Give the position of every Plasmodium parasite and every leukocyte.
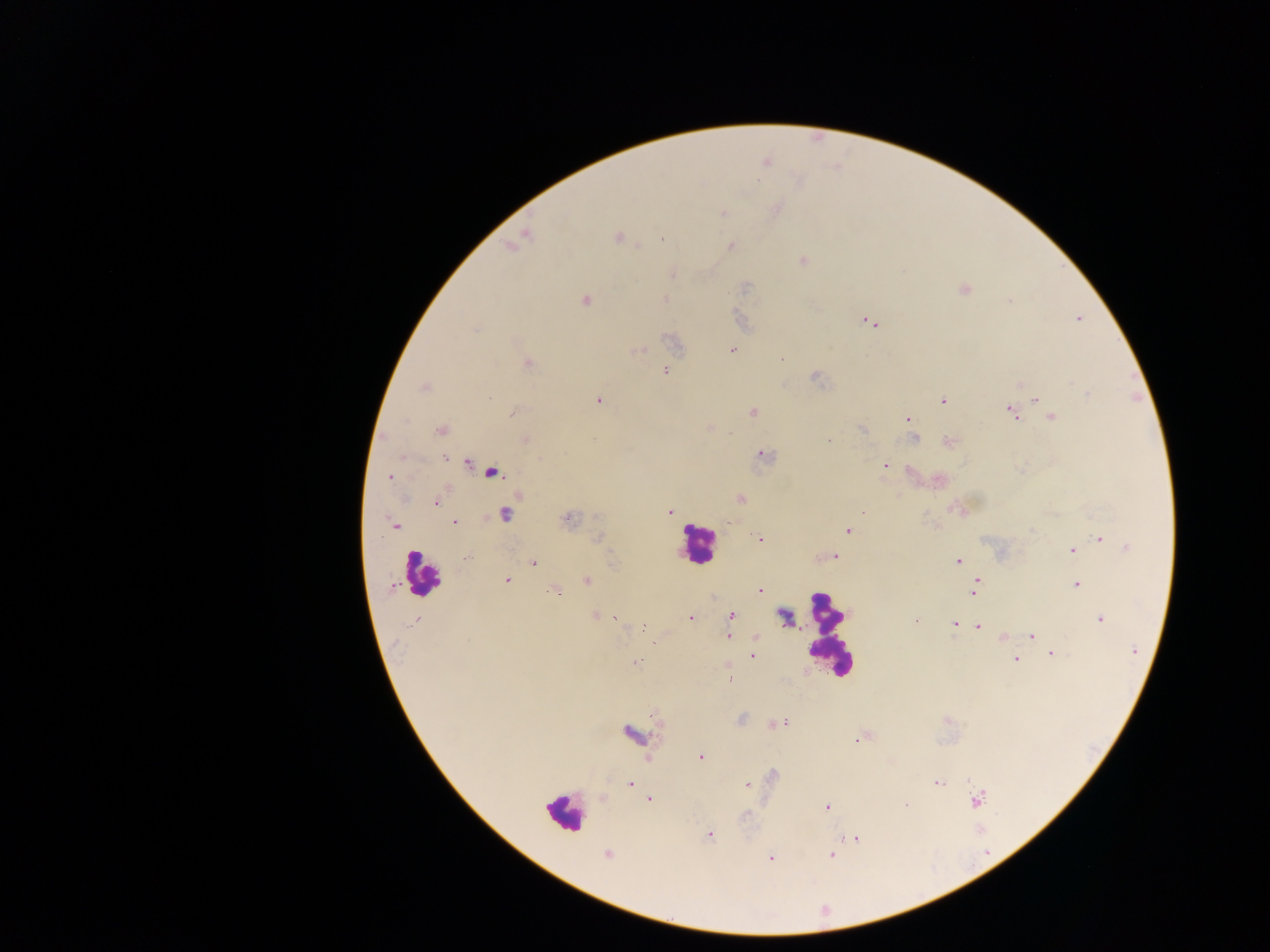
Approximate centers as [x, y] in pixels.
Plasmodium parasites: [723, 213], [527, 236], [617, 238], [638, 246], [731, 246], [803, 261], [672, 274], [964, 290], [664, 299], [585, 301], [1009, 301], [1079, 318], [869, 322], [640, 350], [731, 350], [782, 358], [528, 364], [665, 371], [816, 377], [424, 387], [1088, 394], [1036, 398], [598, 400], [942, 400], [1018, 406], [512, 412], [752, 412], [1011, 413], [1052, 417], [908, 419], [442, 430], [861, 430], [729, 434], [526, 439], [915, 439], [828, 441], [949, 441], [764, 455], [445, 458], [467, 463], [885, 465], [492, 473], [389, 477], [741, 499], [436, 502], [669, 512], [862, 513], [505, 514], [566, 519], [455, 523], [394, 524], [848, 531], [1100, 538], [597, 539], [760, 540], [1126, 547], [1072, 550], [468, 556], [836, 556], [958, 561], [534, 562], [506, 580], [587, 580], [978, 581], [1076, 585], [392, 587], [759, 589], [555, 590], [974, 592], [731, 615], [594, 616], [785, 616], [691, 618], [616, 619], [916, 620], [1100, 620], [954, 624], [977, 627], [645, 628], [1032, 635], [728, 636], [1003, 636], [1134, 650], [1052, 654], [753, 656], [1016, 659], [637, 661], [730, 679], [781, 723], [630, 734], [856, 740], [700, 757], [630, 784], [937, 784], [747, 785], [649, 799], [977, 801], [827, 807], [710, 834], [855, 839], [606, 855], [831, 855], [771, 858].
Leukocytes: [696, 545], [421, 575], [828, 635], [563, 813].

Summary:
  - Capture: mobile-phone photograph through a microscope
  - Image size: 1270×952 pixels
  - Country: Ghana
  - Preparation: thick blood smear
  - Field of view: single